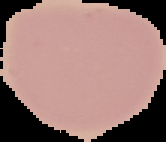

{
  "image_size": "166×142 pixels",
  "image_type": "segmented cell region with the area outside set to black",
  "result": "negative for malaria parasites",
  "preparation": "thin blood smear"
}